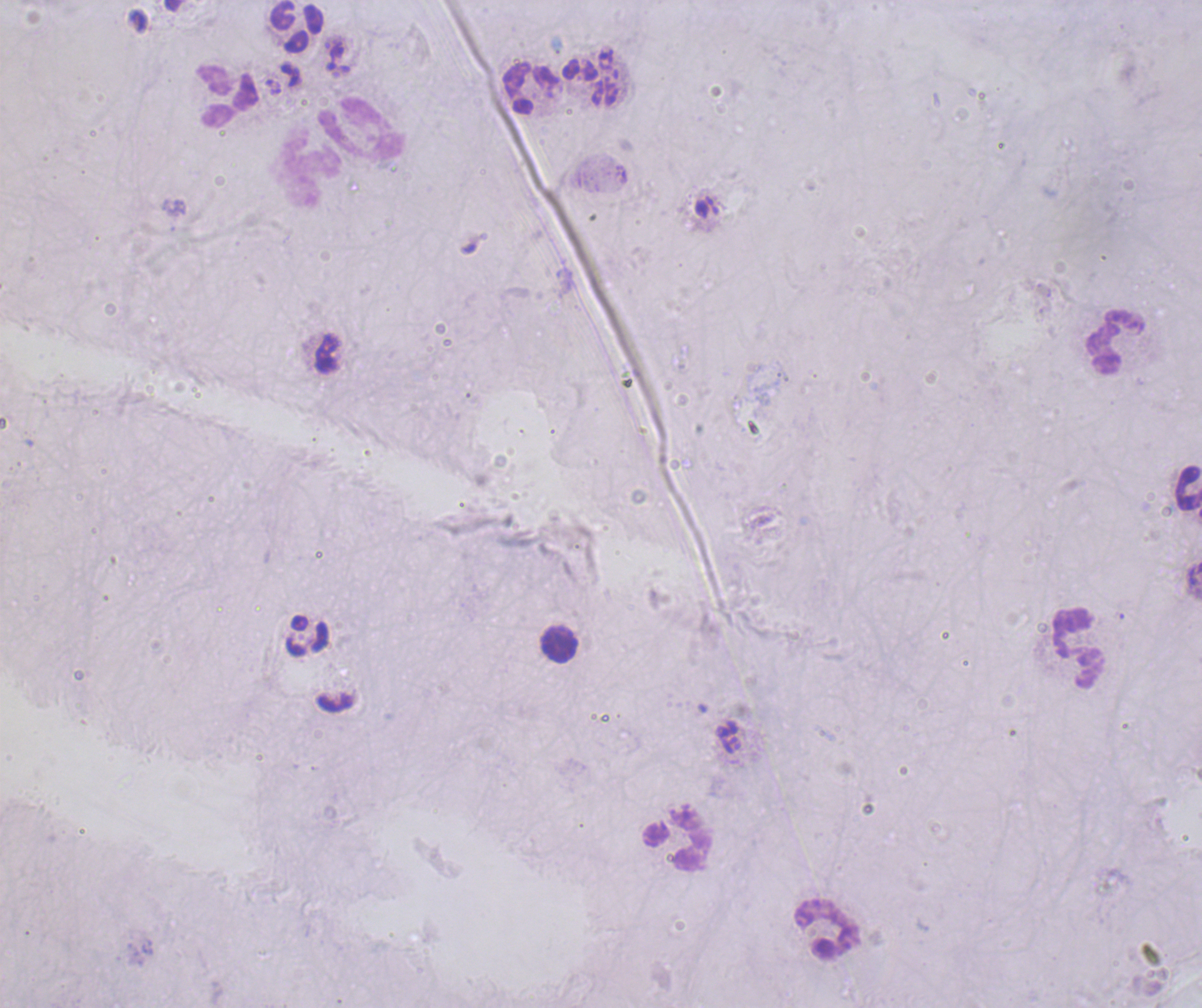
Approximate centers as [x, y] in pixels.
Summary:
  - Leukocyte locations: [297, 26], [530, 88], [228, 96], [361, 129], [310, 167], [1115, 341], [1187, 486], [308, 635], [559, 642], [1078, 645], [676, 838], [829, 930]
  - Image size: 1202×1008 pixels
  - Field of view: one from this slide
  - Background quality: unsatisfactory
  - Coloration quality: bad
  - Magnification: 100x
  - Preparation: thick blood film
  - Stain: Romanowsky
  - Result: negative for malaria parasites
  - Context: previously used in a real diagnosis